Classify this cell by malaria status.
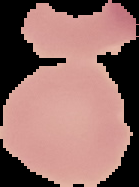
It is uninfected.

image size = 139×187 pixels
image type = segmented cell region on a black background
preparation = thin blood smear